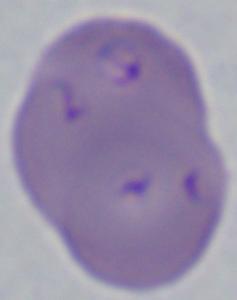

identification = Babesia
magnification = 1000x
modality = micrograph